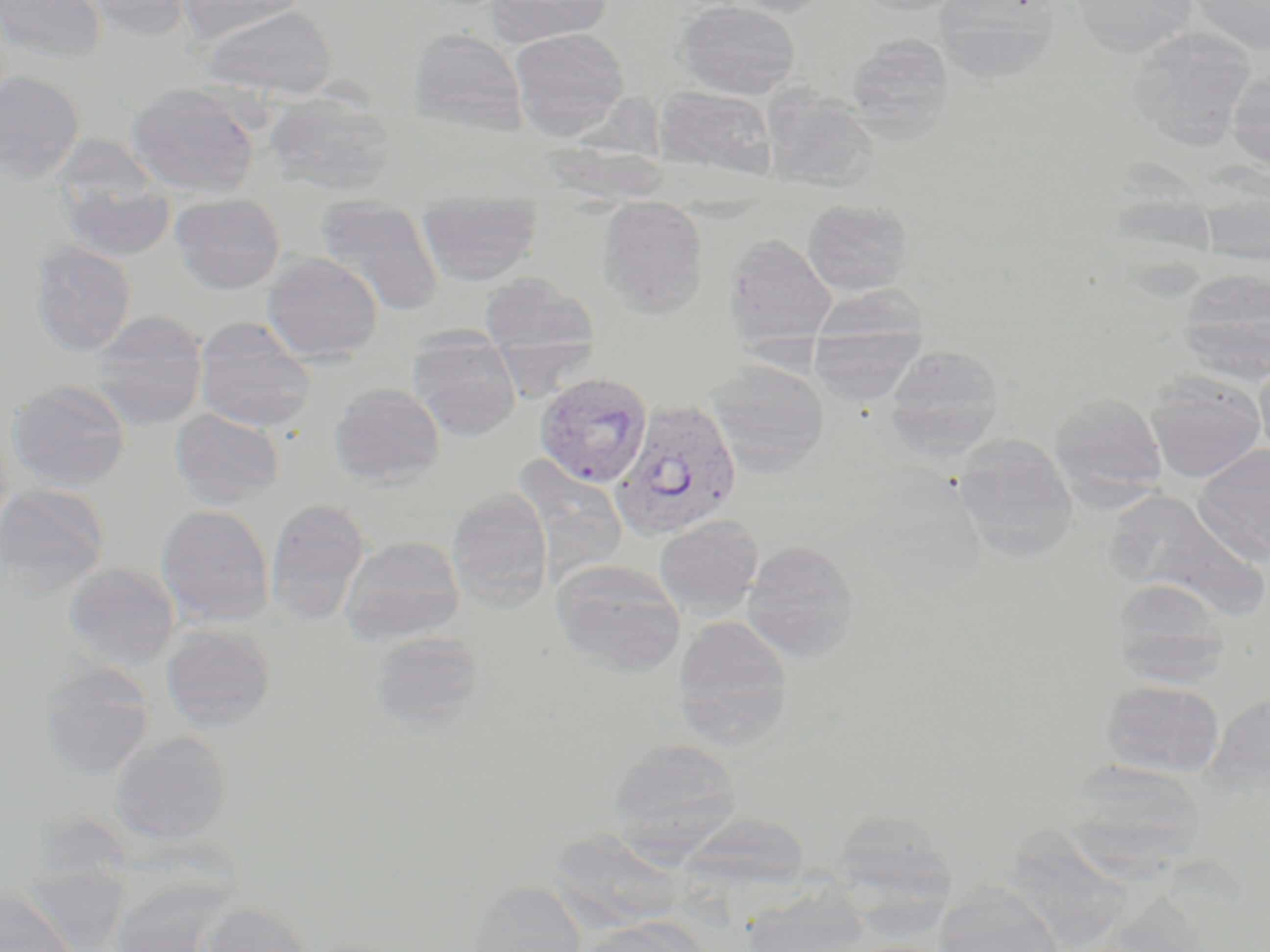

Approximate bounding boxes as named x1/y1/x2/y2 corners in pixels. Uninfected red blood cell locations: (x1=0, y1=0, x2=106, y2=62), (x1=74, y1=0, x2=197, y2=39), (x1=176, y1=0, x2=310, y2=44), (x1=485, y1=0, x2=614, y2=47), (x1=675, y1=0, x2=801, y2=99), (x1=715, y1=0, x2=837, y2=18), (x1=852, y1=0, x2=970, y2=16), (x1=1072, y1=0, x2=1197, y2=58), (x1=1189, y1=0, x2=1270, y2=52), (x1=934, y1=1, x2=1060, y2=84), (x1=197, y1=4, x2=338, y2=100), (x1=1127, y1=27, x2=1257, y2=149), (x1=409, y1=28, x2=527, y2=135), (x1=509, y1=28, x2=629, y2=139), (x1=846, y1=33, x2=953, y2=140), (x1=1227, y1=69, x2=1270, y2=173), (x1=0, y1=70, x2=86, y2=183), (x1=125, y1=82, x2=262, y2=198), (x1=761, y1=85, x2=877, y2=191), (x1=653, y1=86, x2=779, y2=180), (x1=264, y1=91, x2=397, y2=196), (x1=51, y1=133, x2=163, y2=213), (x1=1199, y1=178, x2=1269, y2=268), (x1=58, y1=179, x2=176, y2=262), (x1=169, y1=193, x2=286, y2=294), (x1=802, y1=198, x2=913, y2=296), (x1=314, y1=202, x2=444, y2=315), (x1=596, y1=202, x2=709, y2=317), (x1=417, y1=203, x2=543, y2=284), (x1=724, y1=232, x2=837, y2=350), (x1=28, y1=239, x2=137, y2=356), (x1=262, y1=251, x2=383, y2=365), (x1=1176, y1=269, x2=1270, y2=385), (x1=479, y1=274, x2=599, y2=358), (x1=809, y1=285, x2=927, y2=351), (x1=89, y1=310, x2=208, y2=429), (x1=194, y1=316, x2=317, y2=432), (x1=809, y1=323, x2=926, y2=407), (x1=812, y1=327, x2=983, y2=444), (x1=407, y1=332, x2=522, y2=440), (x1=883, y1=344, x2=1005, y2=459), (x1=1255, y1=358, x2=1270, y2=462), (x1=706, y1=360, x2=830, y2=476), (x1=1145, y1=371, x2=1267, y2=483), (x1=6, y1=379, x2=131, y2=491), (x1=328, y1=383, x2=445, y2=488), (x1=1048, y1=392, x2=1168, y2=509), (x1=169, y1=407, x2=285, y2=509), (x1=952, y1=433, x2=1079, y2=561), (x1=1193, y1=443, x2=1270, y2=566), (x1=511, y1=456, x2=629, y2=582), (x1=0, y1=484, x2=110, y2=596), (x1=446, y1=490, x2=553, y2=612), (x1=1107, y1=490, x2=1267, y2=618), (x1=265, y1=498, x2=371, y2=626), (x1=156, y1=504, x2=275, y2=626), (x1=654, y1=515, x2=763, y2=620), (x1=340, y1=535, x2=465, y2=646), (x1=741, y1=538, x2=860, y2=661), (x1=550, y1=558, x2=686, y2=677), (x1=64, y1=562, x2=181, y2=669), (x1=1111, y1=579, x2=1230, y2=687), (x1=673, y1=614, x2=793, y2=748), (x1=160, y1=623, x2=277, y2=731), (x1=369, y1=630, x2=485, y2=730), (x1=39, y1=660, x2=155, y2=779), (x1=1101, y1=679, x2=1225, y2=778), (x1=110, y1=730, x2=232, y2=844), (x1=607, y1=738, x2=742, y2=852), (x1=1065, y1=765, x2=1205, y2=884), (x1=831, y1=808, x2=953, y2=906), (x1=1007, y1=820, x2=1131, y2=944), (x1=564, y1=834, x2=692, y2=929), (x1=463, y1=881, x2=587, y2=952), (x1=933, y1=884, x2=1065, y2=952), (x1=742, y1=885, x2=872, y2=952), (x1=0, y1=890, x2=78, y2=952), (x1=198, y1=901, x2=314, y2=952), (x1=576, y1=917, x2=707, y2=952). Plasmodium vivax-infected red blood cell locations: (x1=533, y1=372, x2=653, y2=487), (x1=612, y1=398, x2=742, y2=542). Slide-level diagnosis: Plasmodium vivax. Thin blood film. Captured at 1000x magnification. Single field of view. Image is 1270×952 pixels. May-Grünwald-Giemsa stain. Light microscopy.